State which cell type is depicted.
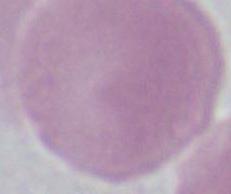
An erythrocyte.

Summary:
  - Modality: micrograph
  - Magnification: 1000x